Draw a bounding box around every Plasmodium parasite.
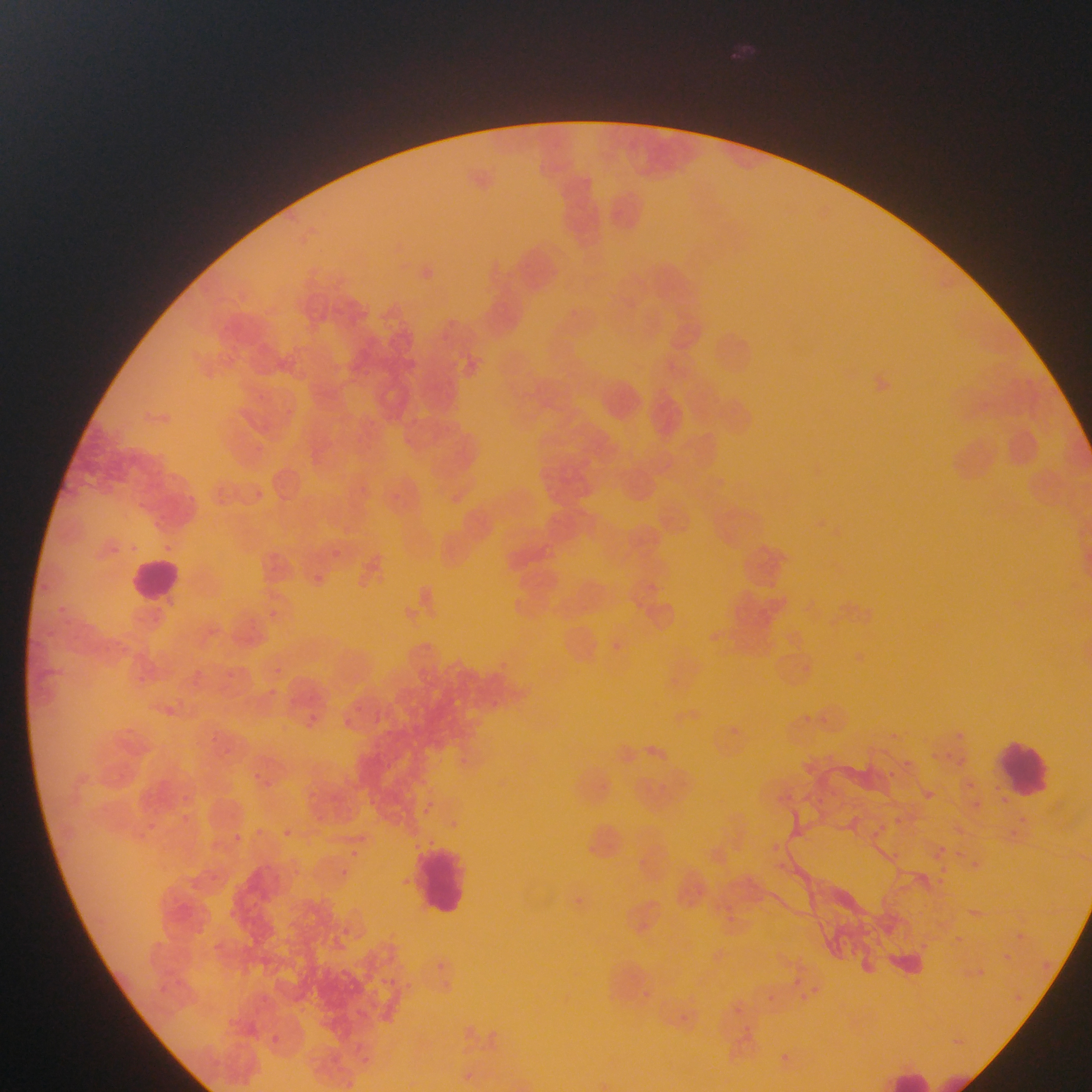

Approximate bounding boxes as (left, top, right, bottom) in pixels.
Plasmodium parasites: (256, 492, 264, 499), (331, 549, 341, 558), (314, 574, 323, 583), (273, 665, 283, 676), (186, 667, 204, 685), (136, 673, 146, 680), (267, 687, 279, 697), (354, 700, 368, 714), (304, 713, 318, 727), (340, 714, 354, 728), (207, 734, 218, 741), (460, 752, 475, 767), (247, 771, 267, 785), (425, 797, 432, 807), (1001, 798, 1009, 805), (973, 801, 980, 809), (421, 809, 430, 820), (182, 812, 190, 821), (150, 821, 157, 833), (252, 825, 268, 834), (281, 825, 294, 838), (355, 829, 367, 843), (232, 831, 242, 840), (343, 848, 357, 858), (334, 869, 350, 877), (207, 870, 217, 880), (399, 876, 414, 887), (576, 894, 586, 904), (228, 906, 245, 922), (343, 923, 353, 933), (434, 958, 444, 969), (383, 973, 399, 984), (407, 981, 416, 989), (769, 984, 781, 1005), (638, 986, 656, 999), (735, 1003, 745, 1017), (670, 1015, 689, 1023), (744, 1023, 755, 1031), (269, 1032, 286, 1042), (350, 1045, 363, 1057), (361, 1053, 382, 1063).

preparation = thin blood smear
field of view = single
image size = 1092×1092 pixels
capture = mobile-phone photograph through a microscope
country = Ghana
leukocyte locations = approximate bounding boxes as (left, top, right, bottom) in pixels: (130, 555, 185, 606), (997, 737, 1055, 800), (413, 841, 471, 920), (890, 1070, 938, 1092)